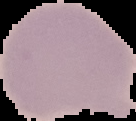
Summary:
  - Image size: 136×121 pixels
  - Malaria status: uninfected
  - Image type: segmented cell region on a black background
  - Preparation: thin blood film